Assess for parasitized red blood cells.
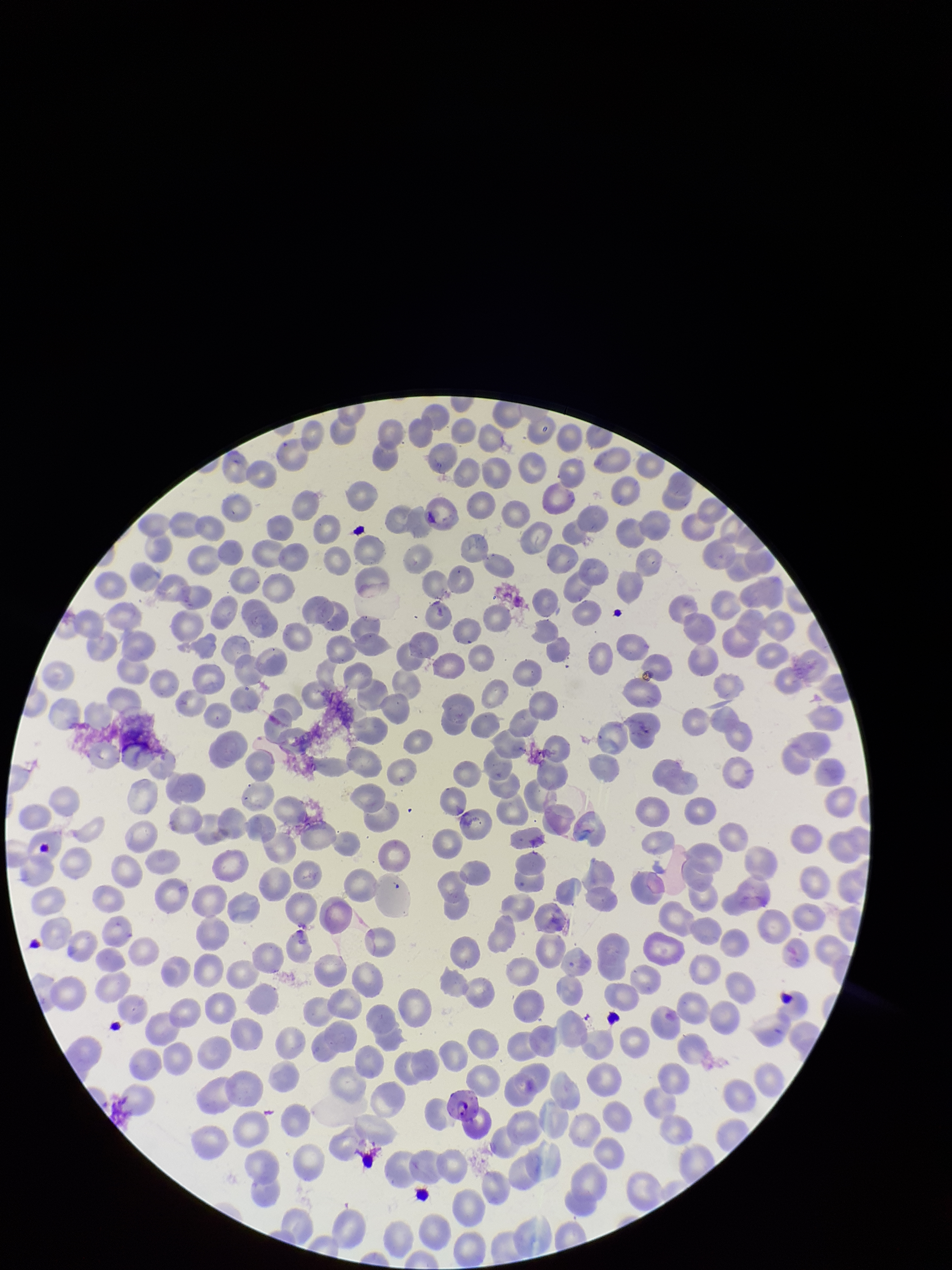

Identified.

preparation = thin smear
parasitized red blood cell count = 2
stain = Giemsa
image size = 952×1270 pixels
red blood cell count = 312
patient malaria status = positive
field of view = single
species reported for this patient = Plasmodium falciparum
capture = smartphone photograph through the microscope eyepiece